Outline each blood parasite and name the species.
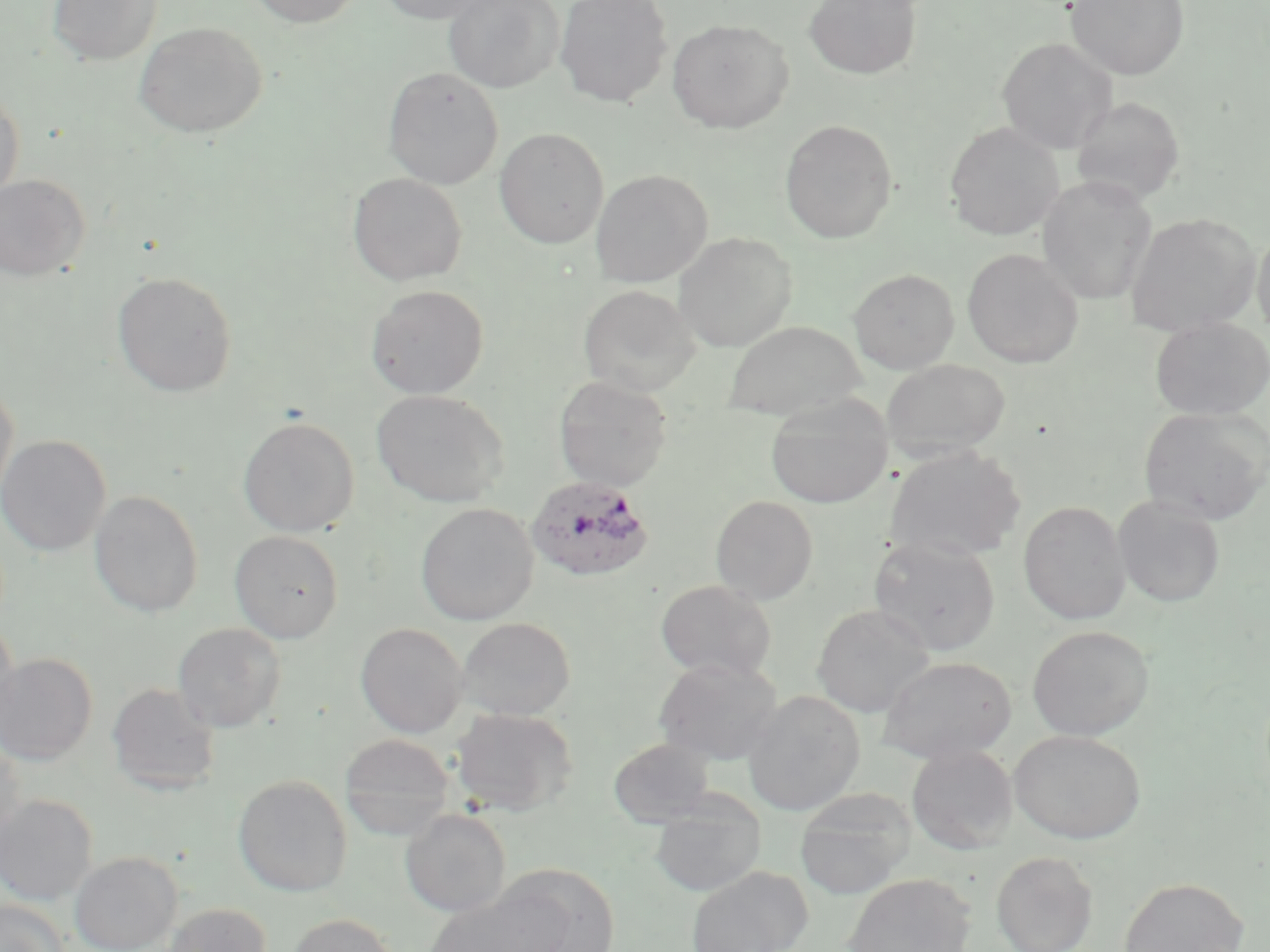
Approximate bounding boxes as (x1, y1, x2, y2) in pixels.
Plasmodium ovale-infected red blood cells: (525, 475, 657, 582).
No Plasmodium falciparum, Plasmodium malariae, Plasmodium vivax, Babesia divergens, or Trypanosoma brucei observed.

{
  "slide_level_diagnosis": "Plasmodium ovale",
  "stain": "May-Grünwald-Giemsa",
  "uninfected_red_blood_cell_locations": "approximate bounding boxes as (x1, y1, x2, y2) in pixels: (46, 0, 162, 65), (246, 0, 364, 27), (375, 0, 496, 24), (443, 0, 564, 93), (555, 0, 672, 106), (803, 0, 923, 80), (1066, 0, 1189, 80), (667, 18, 793, 133), (133, 22, 267, 138), (997, 37, 1117, 154), (382, 67, 503, 189), (0, 88, 25, 203), (1071, 96, 1185, 206), (779, 119, 898, 243), (944, 122, 1064, 240), (494, 127, 609, 248), (590, 169, 712, 287), (348, 172, 467, 286), (0, 174, 90, 281), (1037, 175, 1157, 305), (1125, 213, 1260, 337), (1251, 226, 1270, 339), (673, 232, 798, 350), (962, 248, 1084, 367), (849, 268, 959, 373), (111, 271, 238, 398), (366, 284, 489, 399), (577, 284, 701, 397), (1149, 317, 1270, 419), (723, 320, 865, 420), (881, 358, 1012, 462), (553, 375, 673, 491), (0, 379, 19, 506), (371, 389, 509, 507), (765, 396, 894, 508), (1138, 407, 1269, 525), (238, 416, 359, 536), (0, 434, 111, 556), (885, 446, 1026, 562), (89, 490, 204, 617), (710, 495, 819, 604), (1112, 495, 1226, 608), (1018, 501, 1131, 624), (415, 503, 538, 626), (229, 530, 344, 642), (869, 536, 1001, 656), (655, 579, 777, 682), (812, 603, 935, 717), (457, 616, 576, 720), (0, 622, 20, 739), (172, 622, 286, 732), (356, 623, 468, 737), (1027, 625, 1153, 740), (0, 653, 97, 765), (654, 656, 784, 765), (878, 656, 1017, 763), (107, 682, 221, 795), (743, 690, 865, 816), (450, 706, 578, 816), (1009, 729, 1145, 843), (339, 733, 455, 837), (0, 737, 25, 852), (608, 737, 715, 828), (907, 744, 1018, 854), (233, 774, 352, 897), (795, 791, 914, 898), (0, 794, 98, 905), (649, 795, 766, 897), (400, 807, 511, 916), (69, 850, 183, 952), (991, 851, 1098, 952), (492, 864, 620, 951), (685, 866, 812, 952), (843, 873, 975, 952), (1117, 876, 1249, 952), (422, 886, 568, 952), (0, 899, 69, 952), (162, 903, 270, 952), (287, 912, 397, 952)",
  "image_size": "1270×952 pixels",
  "field_of_view": "single",
  "magnification": "1000x",
  "modality": "light microscopy",
  "preparation": "thin blood smear"
}